Name the parasite shown.
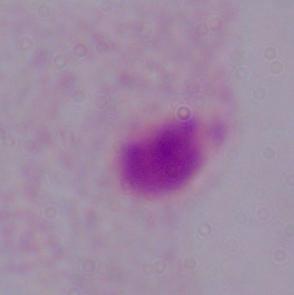
This is a trichomonad.

modality = micrograph
magnification = 1000x